Give the extent of all Plasmodium malariae-infected red blood cells.
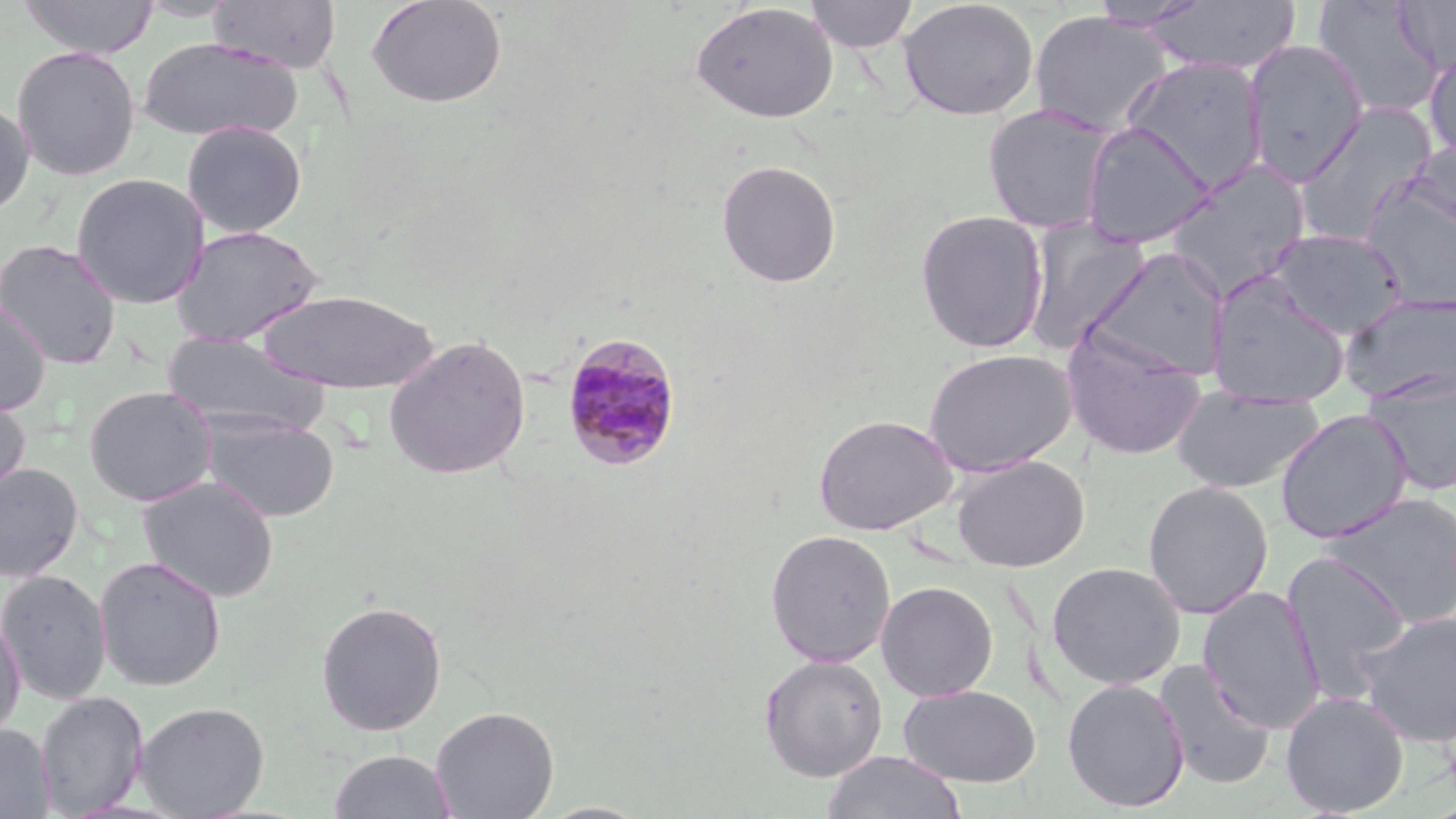
Approximate bounding boxes as (x1, y1, x2, y2) in pixels.
Plasmodium malariae-infected red blood cells: (560, 331, 683, 472).

Summary:
  - Uninfected red blood cell locations: (18, 0, 159, 58), (207, 0, 341, 73), (365, 0, 507, 109), (897, 0, 1039, 121), (1311, 0, 1446, 119), (1392, 0, 1456, 76), (804, 1, 920, 53), (1085, 1, 1207, 31), (1141, 1, 1301, 75), (690, 2, 839, 123), (1028, 11, 1174, 136), (138, 36, 306, 142), (1243, 39, 1368, 185), (1424, 44, 1456, 164), (11, 45, 142, 181), (1121, 56, 1267, 193), (0, 97, 36, 218), (1294, 103, 1439, 244), (982, 104, 1118, 235), (181, 120, 308, 239), (1081, 121, 1215, 249), (1405, 140, 1456, 237), (1165, 158, 1312, 299), (715, 159, 842, 288), (70, 172, 210, 309), (1360, 177, 1456, 311), (915, 209, 1049, 354), (1022, 219, 1150, 353), (171, 224, 323, 347), (1267, 228, 1408, 339), (0, 239, 123, 369), (1082, 246, 1231, 384), (1207, 273, 1352, 408), (260, 290, 439, 393), (1339, 291, 1456, 405), (0, 296, 51, 416), (1061, 328, 1206, 459), (161, 331, 330, 438), (384, 334, 531, 480), (922, 348, 1078, 476), (1363, 371, 1456, 496), (84, 385, 217, 506), (1171, 386, 1324, 494), (0, 390, 31, 499), (1275, 409, 1413, 544), (203, 413, 339, 522), (813, 414, 957, 535), (951, 455, 1089, 572), (0, 463, 83, 582), (138, 474, 279, 603), (1142, 480, 1273, 620), (1320, 492, 1456, 629), (765, 529, 897, 667), (1280, 550, 1412, 701), (94, 555, 227, 691), (1046, 561, 1186, 690), (0, 569, 112, 705), (876, 581, 998, 701), (1197, 587, 1326, 732), (315, 600, 448, 736), (1357, 610, 1456, 747), (0, 611, 26, 742), (759, 653, 888, 781), (1152, 660, 1276, 790), (1062, 678, 1190, 812), (898, 684, 1041, 787), (36, 691, 148, 817), (1280, 691, 1410, 817), (135, 701, 269, 818), (430, 706, 559, 819), (0, 723, 55, 818), (328, 749, 458, 819), (821, 750, 968, 819), (533, 801, 653, 818)
  - Slide-level diagnosis: Plasmodium malariae
  - Modality: light microscopy
  - Magnification: 1000x
  - Image size: 1456×819 pixels
  - Field of view: one of a larger specimen
  - Preparation: thin blood film
  - Stain: May-Grünwald-Giemsa